State which parasite is depicted.
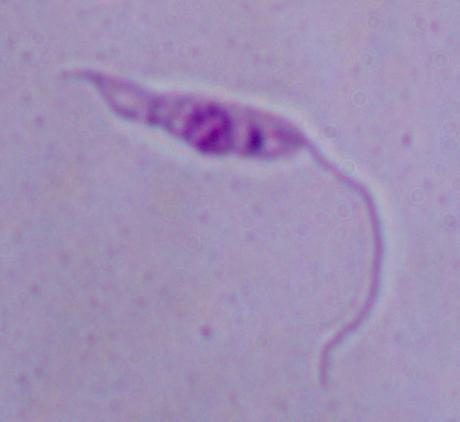
This is Leishmania.

magnification = 1000x
modality = photomicrograph